Mark where platelets are.
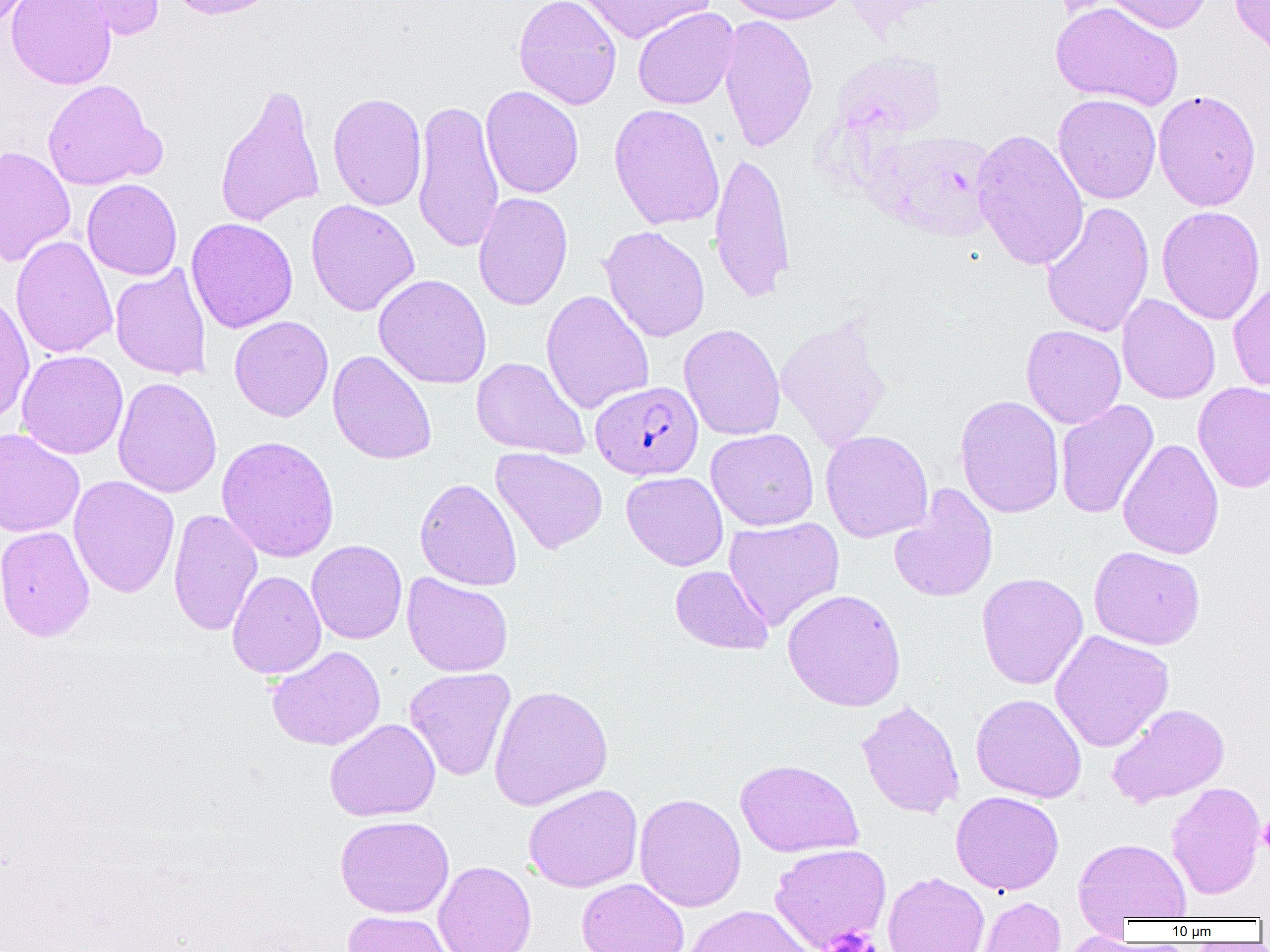

Approximate bounding boxes as (x1,y1)-(x2,y2) corner pairs in pixels.
Platelets: (1257,815)-(1270,857), (822,926)-(879,952).

Uninfected red blood cell locations: (6,0)-(117,90), (57,0)-(165,41), (163,0)-(284,20), (513,0)-(622,109), (576,0)-(713,44), (724,0)-(853,25), (1104,0)-(1213,34), (1229,0)-(1270,62), (1050,2)-(1184,111), (632,7)-(739,110), (718,14)-(818,153), (41,78)-(164,191), (215,82)-(326,229), (481,85)-(583,199), (1153,89)-(1262,211), (327,92)-(427,211), (1052,94)-(1162,204), (412,98)-(505,255), (608,104)-(725,230), (971,128)-(1090,271), (871,129)-(1000,242), (0,146)-(76,267), (709,150)-(796,304), (82,178)-(183,281), (472,192)-(573,311), (306,199)-(420,316), (1041,201)-(1155,338), (1156,205)-(1266,325), (185,218)-(298,333), (599,226)-(710,343), (10,235)-(118,360), (110,265)-(212,381), (373,274)-(492,389), (1227,278)-(1270,393), (541,289)-(655,415), (0,291)-(35,424), (1117,294)-(1221,405), (775,311)-(893,453), (229,315)-(334,422), (678,323)-(786,441), (1021,325)-(1127,429), (16,350)-(128,459), (327,350)-(437,465), (471,356)-(591,461), (113,376)-(222,498), (1193,381)-(1270,494), (954,395)-(1065,518), (1055,399)-(1159,519), (0,428)-(85,538), (706,428)-(819,531), (820,430)-(933,543), (216,435)-(339,563), (1117,438)-(1224,560), (490,447)-(608,554), (622,471)-(728,571), (68,475)-(180,598), (415,477)-(522,591), (889,484)-(998,603), (168,509)-(263,637), (723,516)-(845,630), (0,525)-(95,642), (306,539)-(407,644), (1088,545)-(1206,650), (670,565)-(774,654), (227,570)-(327,680), (976,572)-(1089,689), (401,573)-(514,677), (782,588)-(906,711), (1049,630)-(1174,752), (266,645)-(386,751), (404,667)-(516,781), (487,684)-(613,811), (971,693)-(1087,803), (856,699)-(965,820), (1107,703)-(1230,808), (325,718)-(441,822), (735,759)-(863,857), (1166,781)-(1265,900), (523,783)-(643,893), (951,791)-(1064,895), (634,792)-(746,912), (335,815)-(454,918), (1074,837)-(1192,922), (769,843)-(891,951), (433,860)-(536,952), (882,871)-(990,952), (576,878)-(689,952), (977,897)-(1066,952), (682,905)-(815,952), (342,910)-(456,952), (1060,932)-(1144,952). Plasmodium falciparum-infected red blood cell locations: (591,380)-(703,480). Slide-level diagnosis: Plasmodium falciparum. Thin blood smear. 1000x magnification. Image is 1270×952 pixels. Light microscopy. One field of a larger specimen.